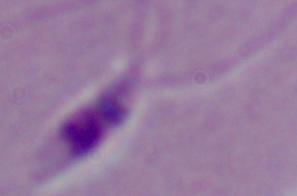
1000x magnification. Photomicrograph. A Leishmania parasite is seen.